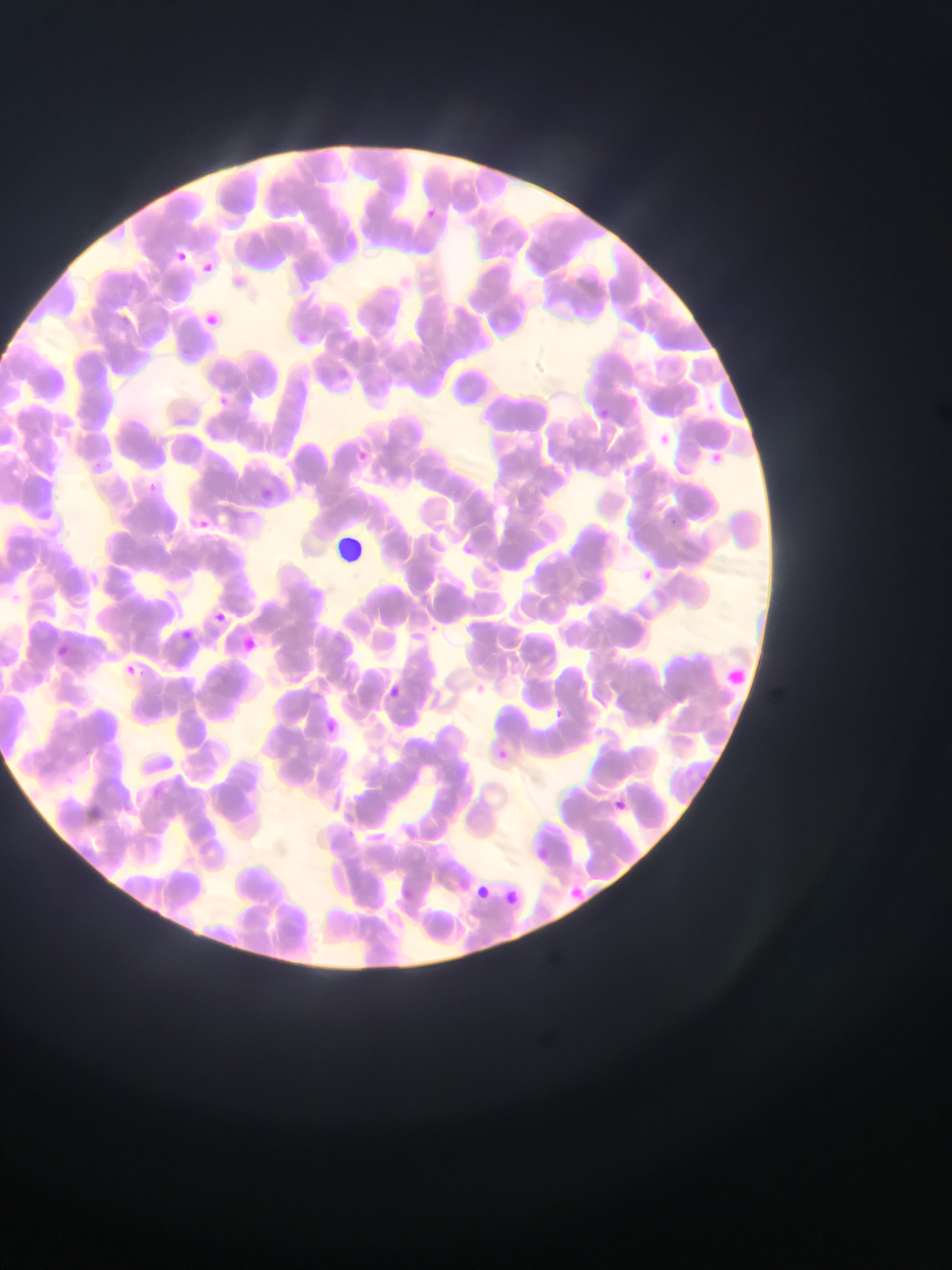

Approximate bounding boxes as (left, top, right, bottom) in pixels.
Summary:
  - Malaria parasite locations: (425, 209, 441, 219), (171, 245, 192, 267), (197, 256, 220, 278), (228, 271, 251, 292), (208, 386, 235, 418), (212, 392, 232, 411), (601, 405, 620, 424), (659, 434, 676, 451), (347, 444, 372, 466), (705, 448, 740, 473), (93, 460, 103, 473), (144, 480, 159, 495), (670, 512, 682, 532), (190, 515, 212, 534), (637, 566, 652, 580), (56, 645, 65, 658), (125, 663, 135, 672), (380, 681, 406, 705), (548, 701, 567, 722), (606, 796, 632, 819)
  - Leukocyte locations: (338, 535, 377, 570), (715, 655, 761, 698)
  - Preparation: thin blood film
  - Capture: mobile-phone photograph through a microscope
  - Country: Ghana
  - Image size: 952×1270 pixels
  - Field of view: single